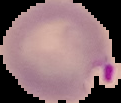
From a thin blood smear. Image is 121×103 pixels. Result: malaria parasites detected. The area outside the segmented cell region is set to black.